Assess the morphology of the red blood cells.
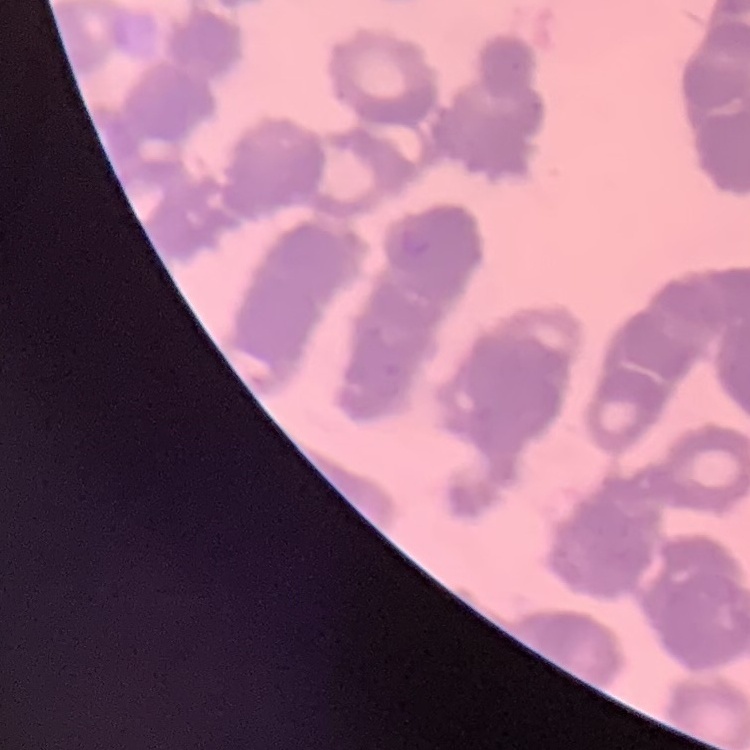

Rouleaux formation.

{
  "preparation": "thin blood smear",
  "image_type": "one tile cut from a larger photomicrograph",
  "stain": "Field's or Giemsa"
}